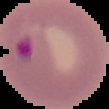
Summary:
  - Preparation: thin blood film
  - Result: malaria parasites detected
  - Image size: 109×109 pixels
  - Image type: segmented cell region with the area outside set to black